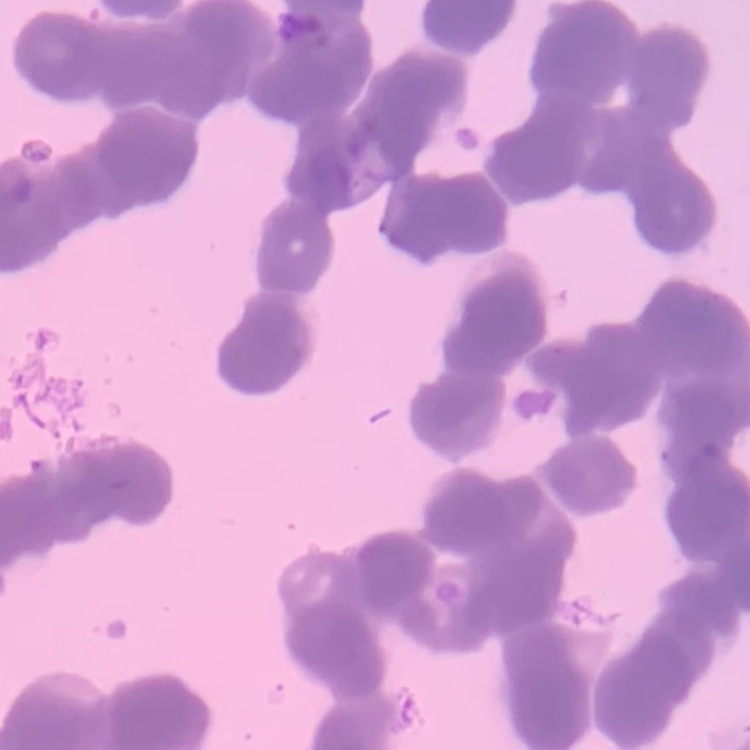
red blood cell morphology = rouleaux formation
image type = one tile cut from a larger photomicrograph
preparation = thin blood smear
stain = Field's or Giemsa